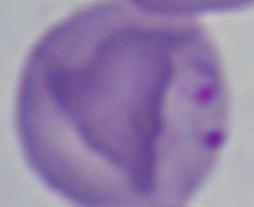
{
  "identification": "Babesia",
  "magnification": "1000x",
  "modality": "micrograph"
}